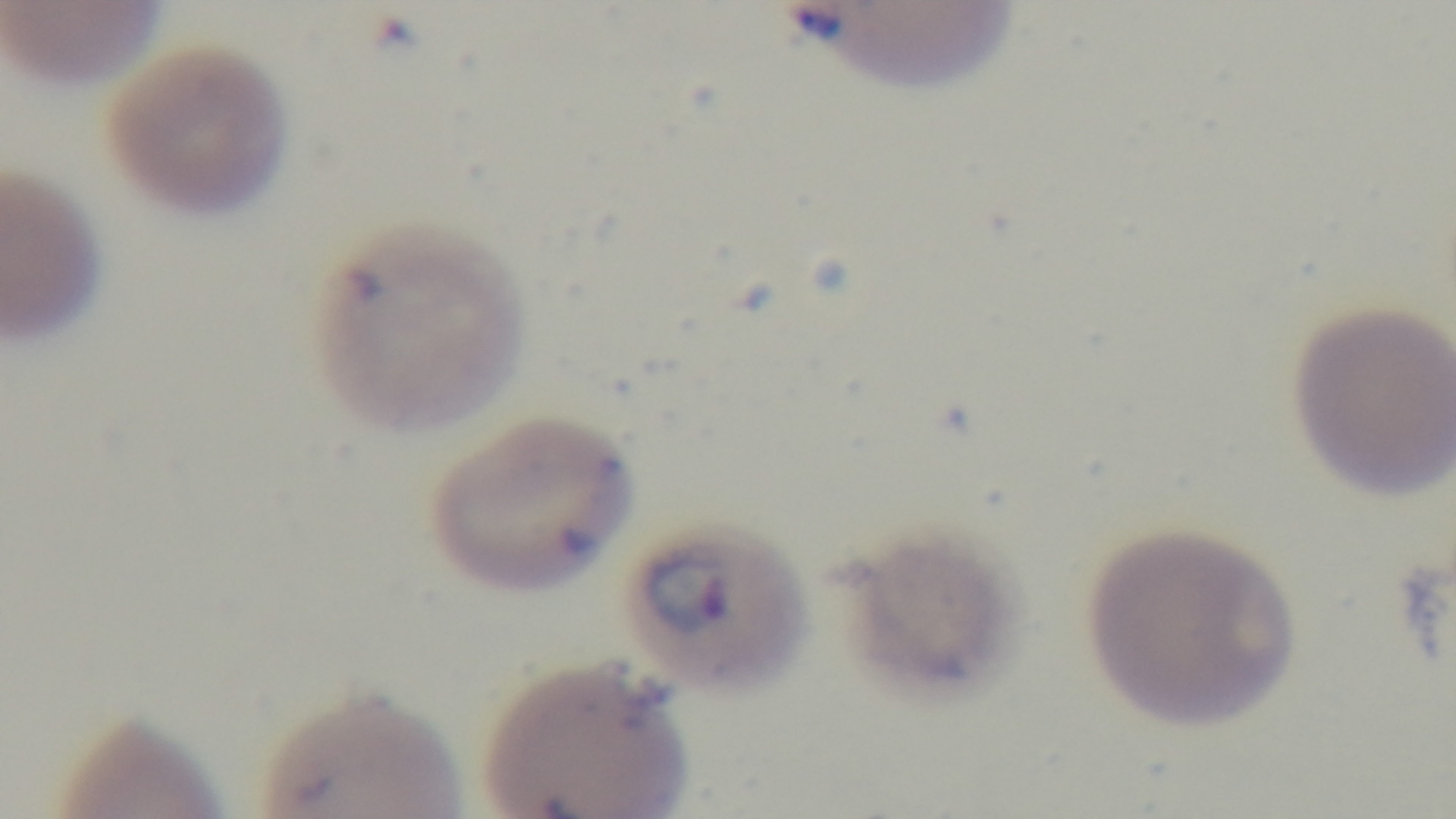
Summary:
  - Modality: light microscopy
  - Malaria status: infected
  - Objective: 100x oil immersion
  - Stain: Giemsa
  - Field of view: one from the slide
  - Preparation: thin blood film
  - Capture: mounted 4K digital camera